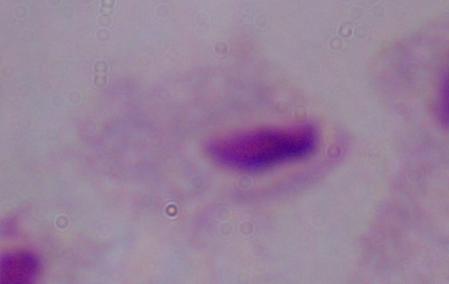
modality: photomicrograph
magnification: 1000x
identification: trichomonad